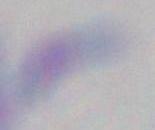

Captured at 1000x magnification. Toxoplasma gondii is shown. Micrograph.